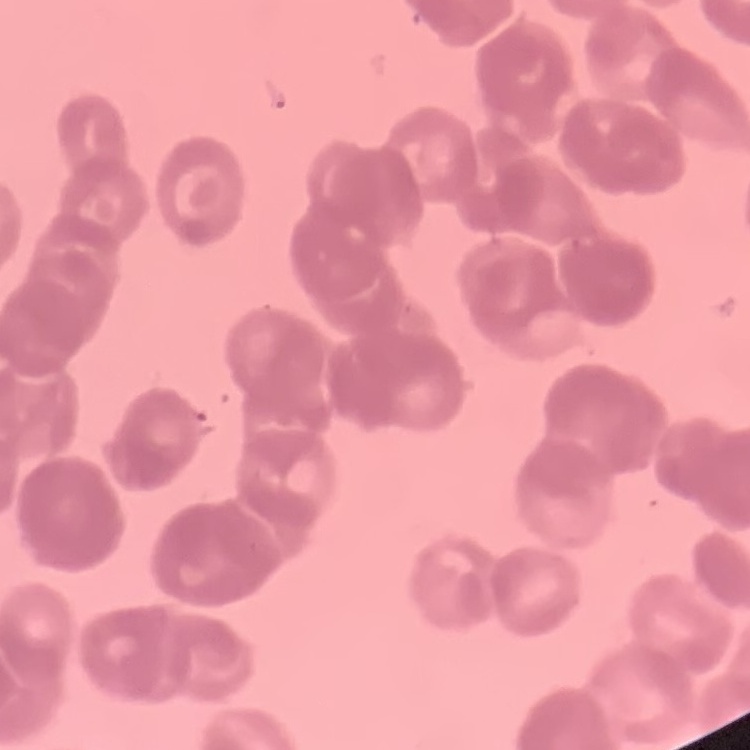

Summary:
  - Erythrocyte morphology: rouleaux formation
  - Image type: one tile cut from a larger photomicrograph
  - Preparation: thin blood smear
  - Stain: Field's or Giemsa